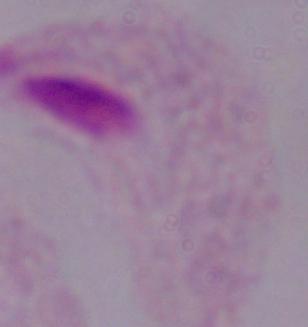

Summary:
  - Magnification: 1000x
  - Identification: trichomonad
  - Modality: photomicrograph